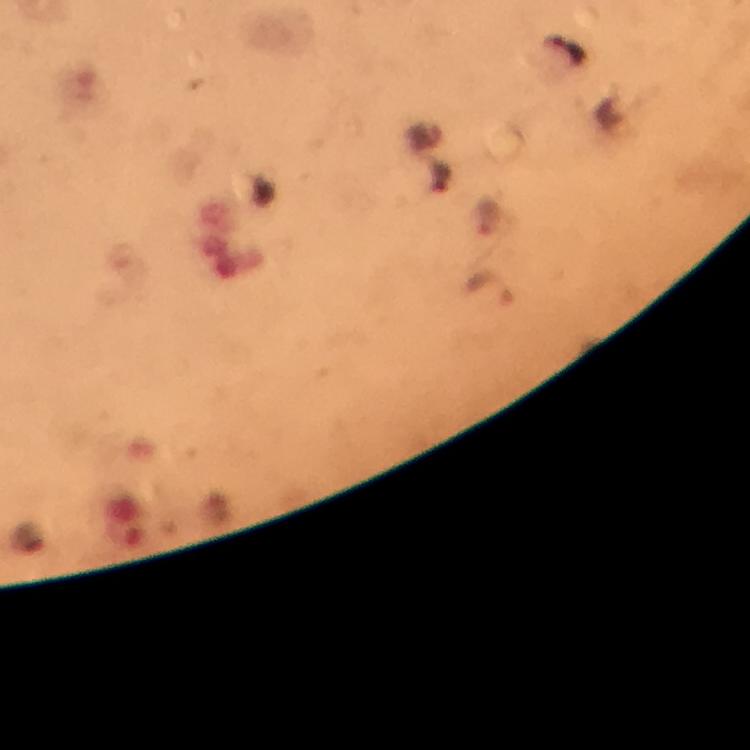

stain = Giemsa
preparation = thick smear
Plasmodium parasite locations = approximate centers as [x, y] in pixels: [489, 288]
capture = smartphone mounted on the microscope
magnification = 100x
cropped from = one field of view
immersion oil = used
context = from a diagnostic examination for malaria
image size = 750×750 pixels